Describe the morphology of the erythrocytes.
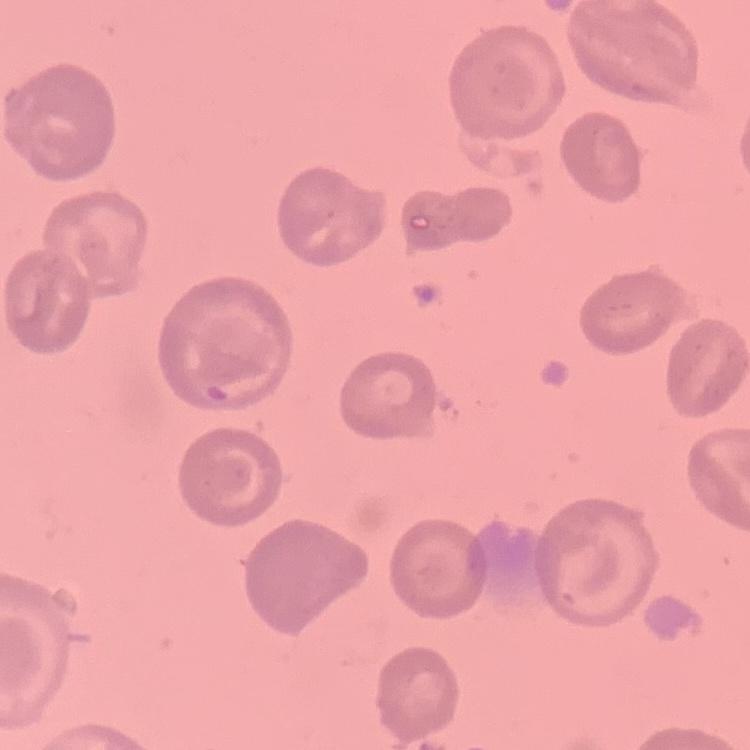
No rouleaux formation.

preparation = thin blood smear
stain = Field's or Giemsa
image type = one tile cut from a larger photomicrograph